Name the parasite shown.
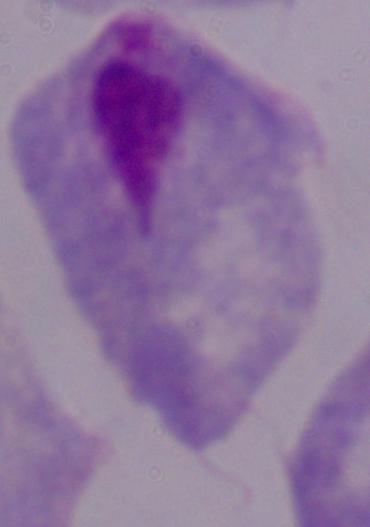

This is a trichomonad.

Captured at 1000x magnification. Photomicrograph.